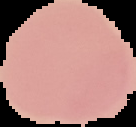
image_type: segmented cell region with the area outside set to black
preparation: thin blood smear
image_size: 136×127 pixels
malaria_status: uninfected